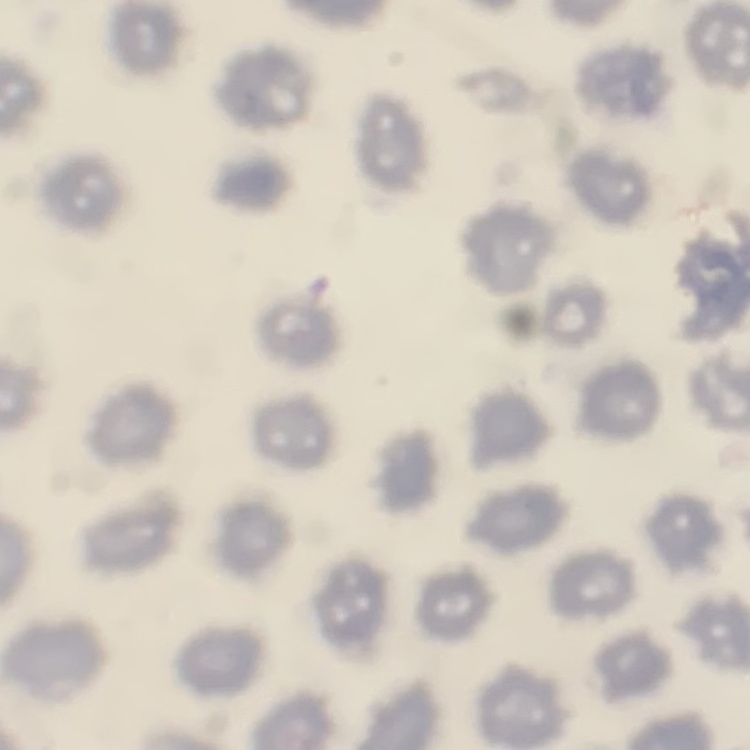

Summary:
  - Red blood cell morphology: no rouleaux formation
  - Image type: square crop of a larger photomicrograph
  - Preparation: thin blood smear
  - Stain: Field's or Giemsa